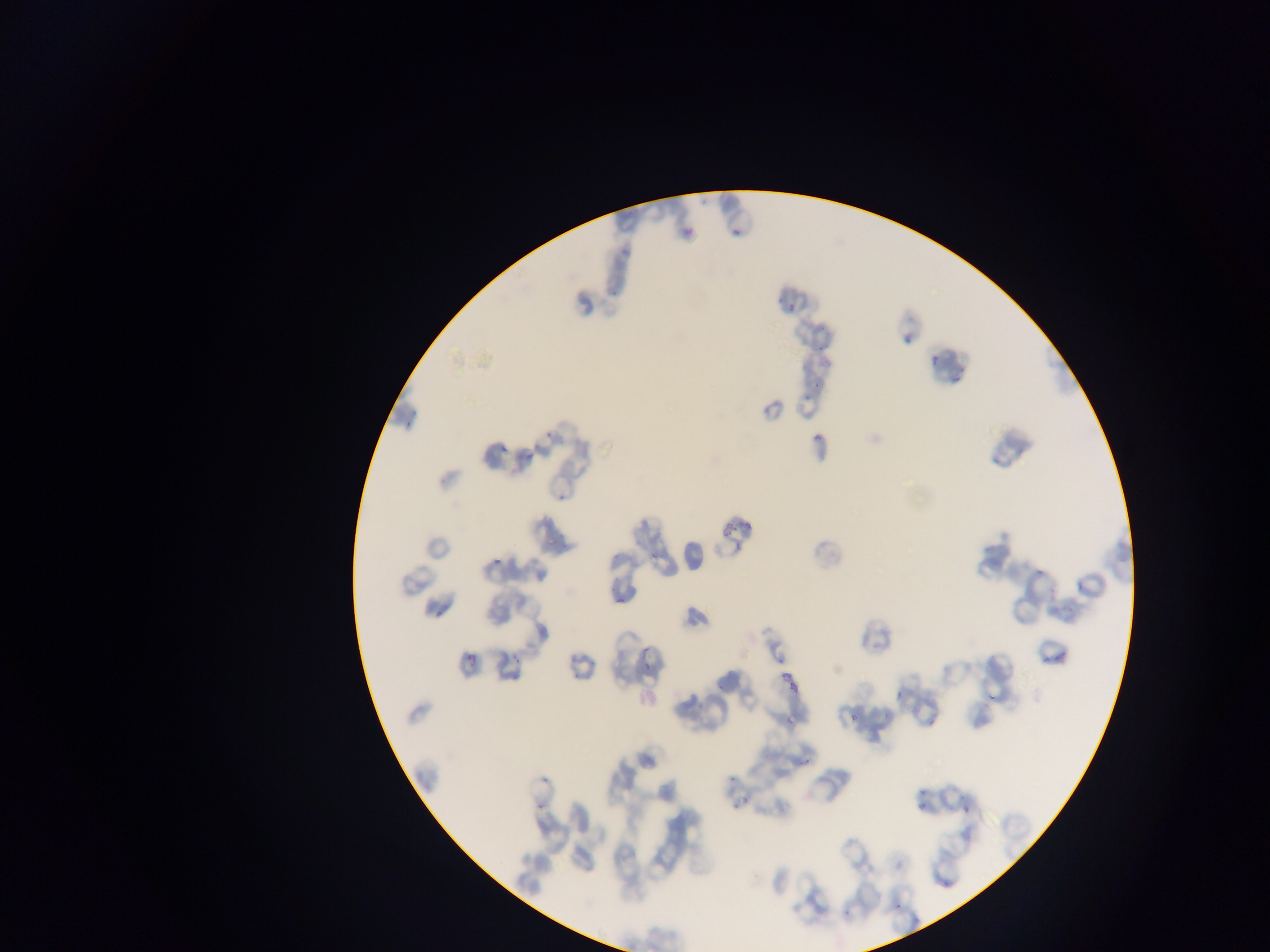

{
  "preparation": "thin blood film",
  "capture": "mobile-phone photograph through a microscope",
  "country": "Ghana",
  "plasmodium_parasite_locations": "approximate bounding boxes as (left, top, right, bottom) in pixels: (686, 228, 696, 235), (788, 300, 797, 312), (930, 353, 941, 365), (815, 433, 822, 444), (498, 443, 516, 456), (526, 450, 537, 463), (650, 552, 663, 562), (493, 555, 500, 565), (1074, 579, 1083, 591), (614, 596, 624, 604), (1057, 650, 1069, 661), (468, 655, 479, 668), (1042, 656, 1049, 664), (645, 660, 653, 672), (782, 672, 792, 679), (790, 680, 798, 691), (895, 689, 902, 698), (985, 695, 1004, 701), (846, 715, 860, 722), (782, 716, 795, 724), (925, 719, 936, 727), (798, 759, 816, 771), (737, 794, 747, 806), (919, 800, 930, 812), (961, 807, 969, 811), (892, 901, 904, 909) | approximate (x, y) pixel centers of objects too small to bound: (733, 234)",
  "image_size": "1270×952 pixels",
  "field_of_view": "single"
}